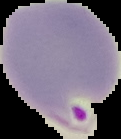

From a thin blood smear. Segmented cell region on a black background. Image is 121×139 pixels. Malaria status: parasitized.